Assess this cell for malaria.
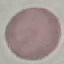

It is uninfected.

Summary:
  - Preparation: thin blood smear
  - Capture: smartphone camera at the microscope eyepiece
  - Image type: cell patch, automatically extracted from a larger field of view and resized to 64 × 64 pixels
  - Stain: Giemsa